Comment on the morphology of the erythrocytes.
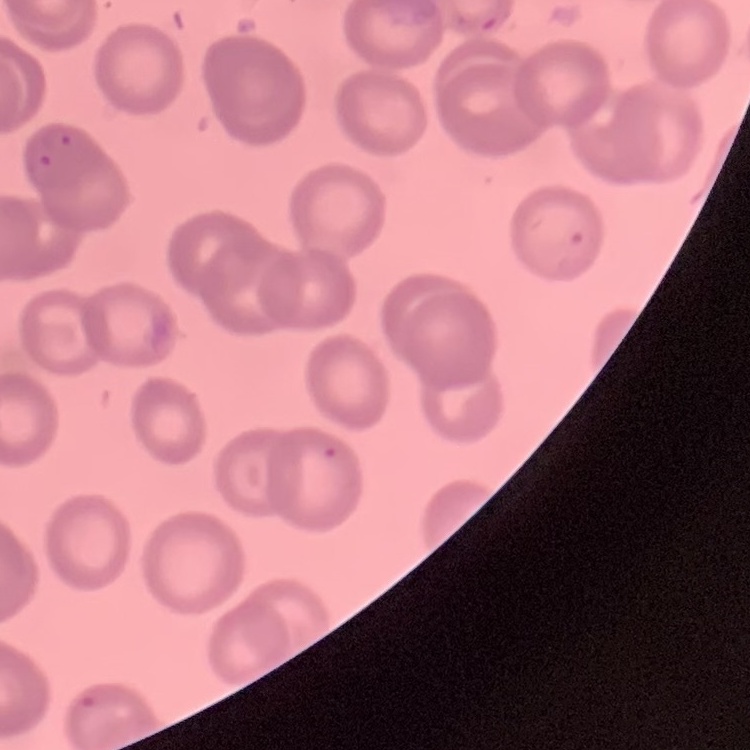

No rouleaux formation.

Summary:
  - Stain: Field's or Giemsa
  - Image type: one tile cut from a larger photomicrograph
  - Preparation: thin blood film